Point out each Plasmodium parasite.
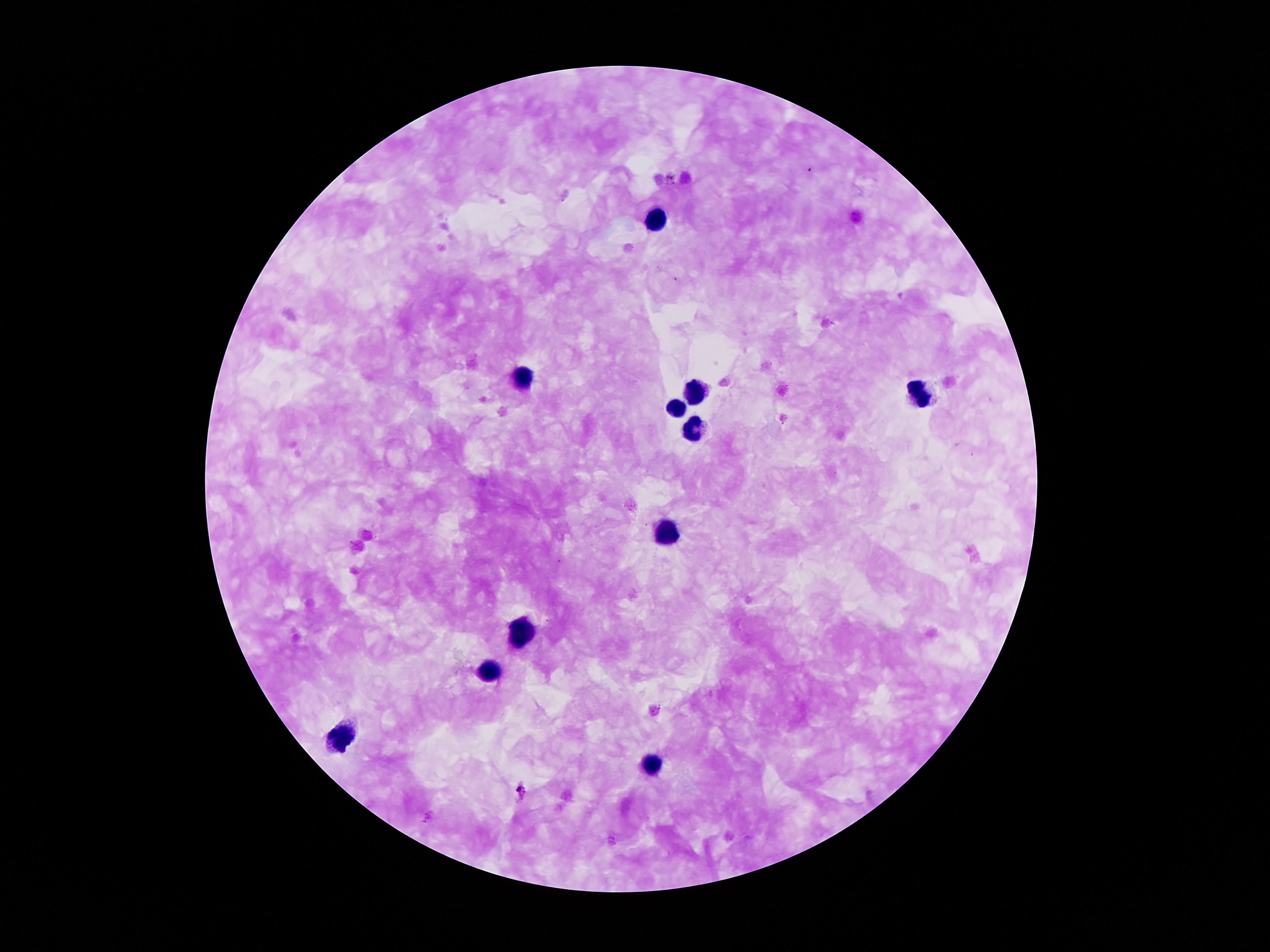
Approximate centers as (x, y) in pixels.
Plasmodium parasites: (521, 792).

Leukocyte locations: (658, 221), (524, 380), (692, 393), (920, 393), (676, 409), (692, 430), (666, 532), (520, 635), (486, 672), (342, 742), (648, 765). Thick peripheral-blood smear. Image is 1270×952 pixels. 100x magnification. One field from this slide. Smartphone photograph taken through the microscope eyepiece. Patient malaria status: positive for Plasmodium falciparum. Giemsa-stained preparation.